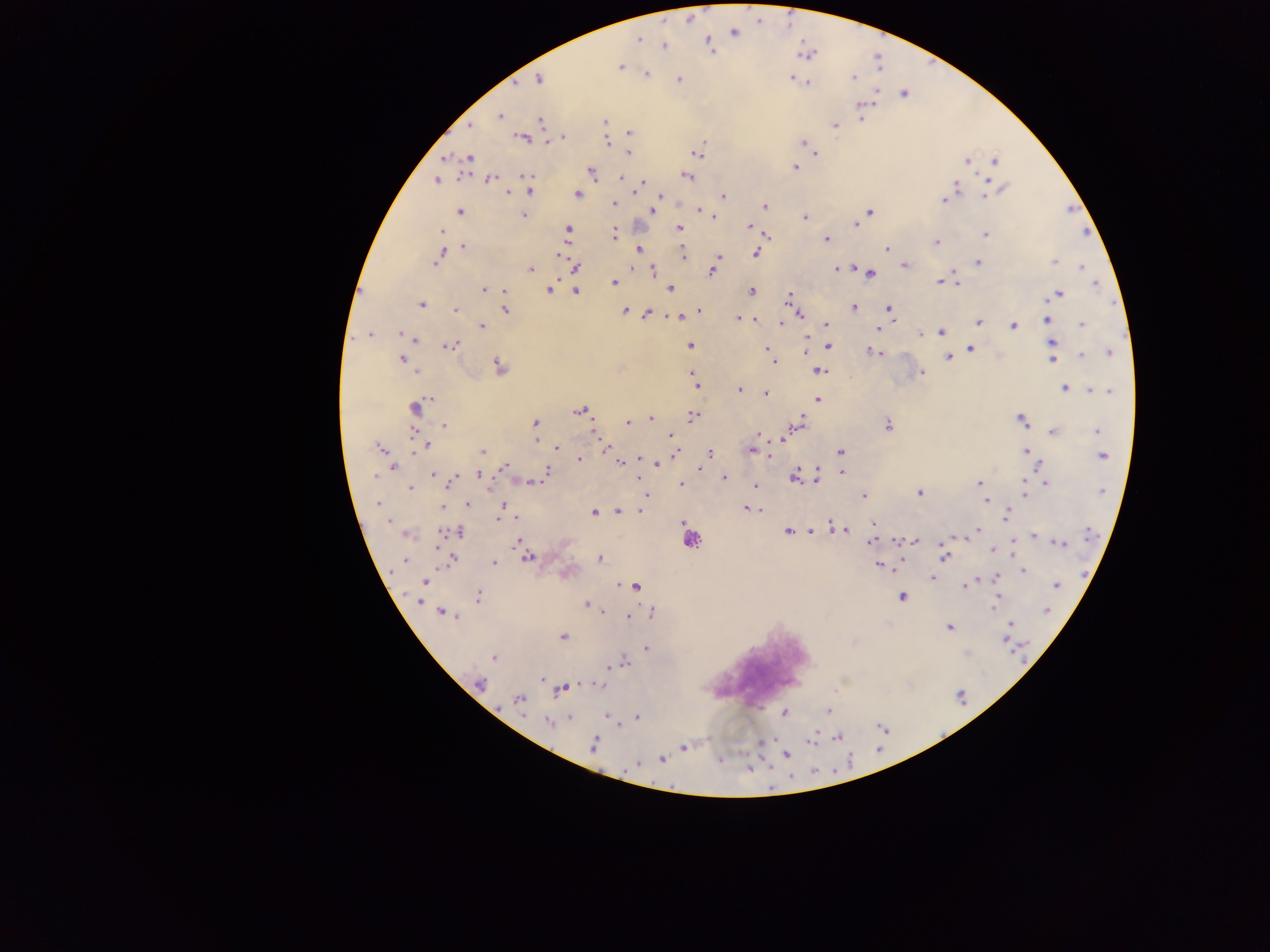 Approximate centers as [x, y] in pixels. Plasmodium parasite locations: [792, 22], [759, 23], [734, 32], [639, 39], [709, 42], [802, 43], [663, 45], [817, 51], [876, 56], [932, 59], [622, 67], [879, 67], [647, 74], [679, 78], [789, 78], [852, 79], [537, 80], [807, 83], [517, 84], [876, 91], [903, 94], [859, 106], [500, 118], [861, 119], [541, 120], [605, 123], [835, 123], [472, 124], [630, 131], [525, 138], [546, 140], [803, 140], [607, 142], [630, 154], [814, 154], [468, 157], [995, 160], [965, 163], [795, 167], [592, 174], [526, 175], [621, 176], [688, 177], [461, 178], [491, 179], [643, 180], [987, 181], [435, 182], [958, 187], [529, 193], [657, 194], [508, 195], [578, 195], [663, 195], [723, 195], [984, 195], [942, 201], [614, 202], [615, 204], [764, 204], [698, 209], [704, 209], [461, 210], [869, 211], [654, 213], [524, 216], [804, 217], [713, 218], [855, 225], [750, 226], [567, 229], [678, 229], [441, 231], [987, 233], [615, 235], [767, 236], [826, 240], [938, 241], [462, 246], [886, 249], [441, 250], [637, 250], [683, 252], [684, 254], [755, 254], [719, 258], [557, 261], [1053, 261], [978, 262], [436, 264], [1082, 265], [836, 267], [845, 267], [904, 267], [576, 268], [530, 269], [951, 270], [865, 271], [653, 272], [711, 272], [871, 274], [956, 278], [940, 281], [958, 281], [614, 282], [1098, 283], [549, 289], [670, 289], [482, 290], [501, 291], [504, 291], [576, 291], [751, 292], [789, 294], [1060, 294], [421, 305], [888, 307], [853, 309], [505, 310], [625, 310], [455, 311], [702, 312], [647, 313], [801, 314], [677, 316], [738, 318], [754, 320], [891, 320], [1046, 320], [979, 322], [1083, 323], [781, 324], [826, 324], [480, 326], [1012, 326], [878, 330], [940, 332], [366, 334], [402, 335], [416, 340], [690, 344], [1051, 344], [451, 345], [828, 345], [766, 348], [971, 348], [871, 349], [1108, 352], [805, 353], [1082, 354], [948, 357], [402, 358], [1052, 361], [772, 362], [498, 364], [814, 369], [923, 370], [821, 371], [694, 382], [698, 385], [1065, 387], [738, 390], [1091, 391], [1101, 391], [765, 392], [1109, 392], [429, 398], [818, 400], [416, 407], [580, 411], [694, 416], [652, 419], [1023, 419], [627, 422], [804, 422], [535, 423], [889, 424], [445, 425], [1098, 431], [1053, 432], [592, 433], [758, 433], [412, 435], [671, 437], [535, 440], [780, 441], [413, 445], [427, 447], [558, 448], [380, 449], [606, 450], [751, 451], [1026, 451], [482, 452], [840, 452], [709, 453], [1102, 455], [637, 456], [769, 456], [579, 457], [619, 464], [502, 465], [658, 465], [393, 468], [701, 470], [548, 471], [842, 472], [433, 474], [477, 474], [819, 474], [794, 475], [816, 477], [453, 478], [723, 478], [374, 479], [792, 480], [978, 482], [1046, 482], [525, 483], [681, 485], [409, 487], [756, 487], [1101, 493], [920, 494], [1025, 495], [646, 496], [862, 497], [986, 501], [376, 503], [467, 504], [503, 505], [442, 507], [745, 507], [618, 511], [640, 511], [594, 513], [1006, 514], [496, 520], [516, 521], [875, 523], [830, 524], [980, 528], [788, 530], [813, 530], [845, 530], [442, 531], [460, 531], [957, 537], [1034, 537], [1043, 537], [897, 542], [914, 542], [949, 542], [1064, 542], [868, 543], [1058, 544], [1012, 548], [991, 553], [600, 558], [528, 559], [944, 559], [405, 561], [455, 561], [495, 561], [901, 561], [877, 566], [1023, 571], [930, 578], [996, 579], [425, 583], [617, 584], [963, 586], [1056, 586], [637, 587], [480, 595], [901, 597], [997, 597], [585, 603], [995, 605], [1045, 611], [440, 612], [602, 612], [458, 616], [628, 616], [1011, 623], [949, 627], [563, 637], [1003, 642], [646, 647], [494, 657], [625, 661], [607, 667], [613, 667], [481, 684], [600, 685], [560, 690], [518, 701], [829, 711], [785, 713], [606, 716], [638, 717], [568, 718], [547, 723], [885, 730], [597, 738], [838, 739], [812, 740], [594, 747], [684, 749], [789, 754], [721, 759], [661, 760], [852, 760], [636, 765], [749, 766], [835, 772]. Thick blood smear. Image is 1270×952 pixels. Collected in Ghana. Single field of view. Photographed through a microscope with a mobile-phone camera.